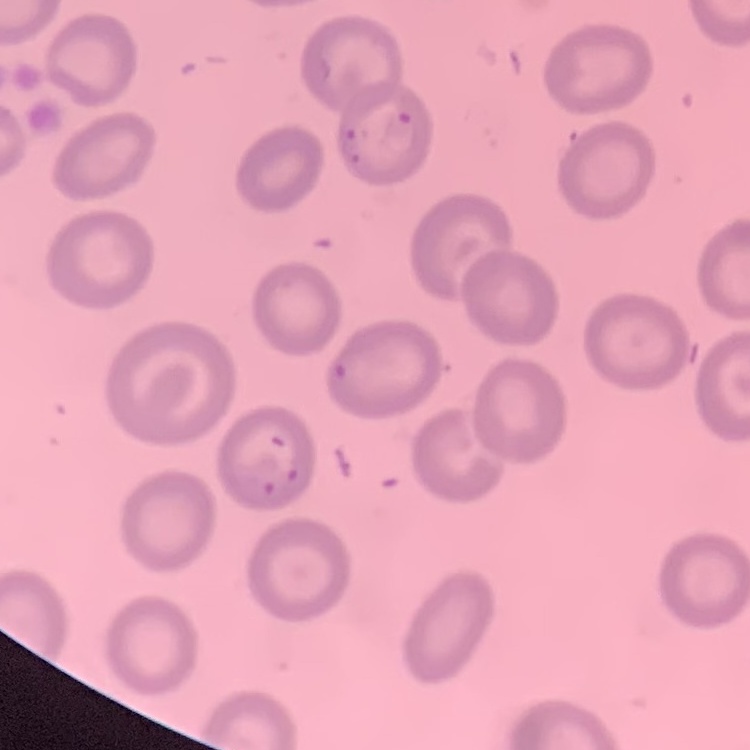
erythrocyte_morphology: no rouleaux formation
preparation: thin blood film
image_type: one tile cut from a larger photomicrograph
stain: Field's or Giemsa